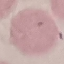
{
  "result": "no malaria parasites seen",
  "preparation": "thin blood smear",
  "image_type": "automatically extracted cell patch, resized to 64 × 64 pixels",
  "stain": "Giemsa",
  "capture": "smartphone through the microscope eyepiece"
}